Outline each blood parasite and name the species.
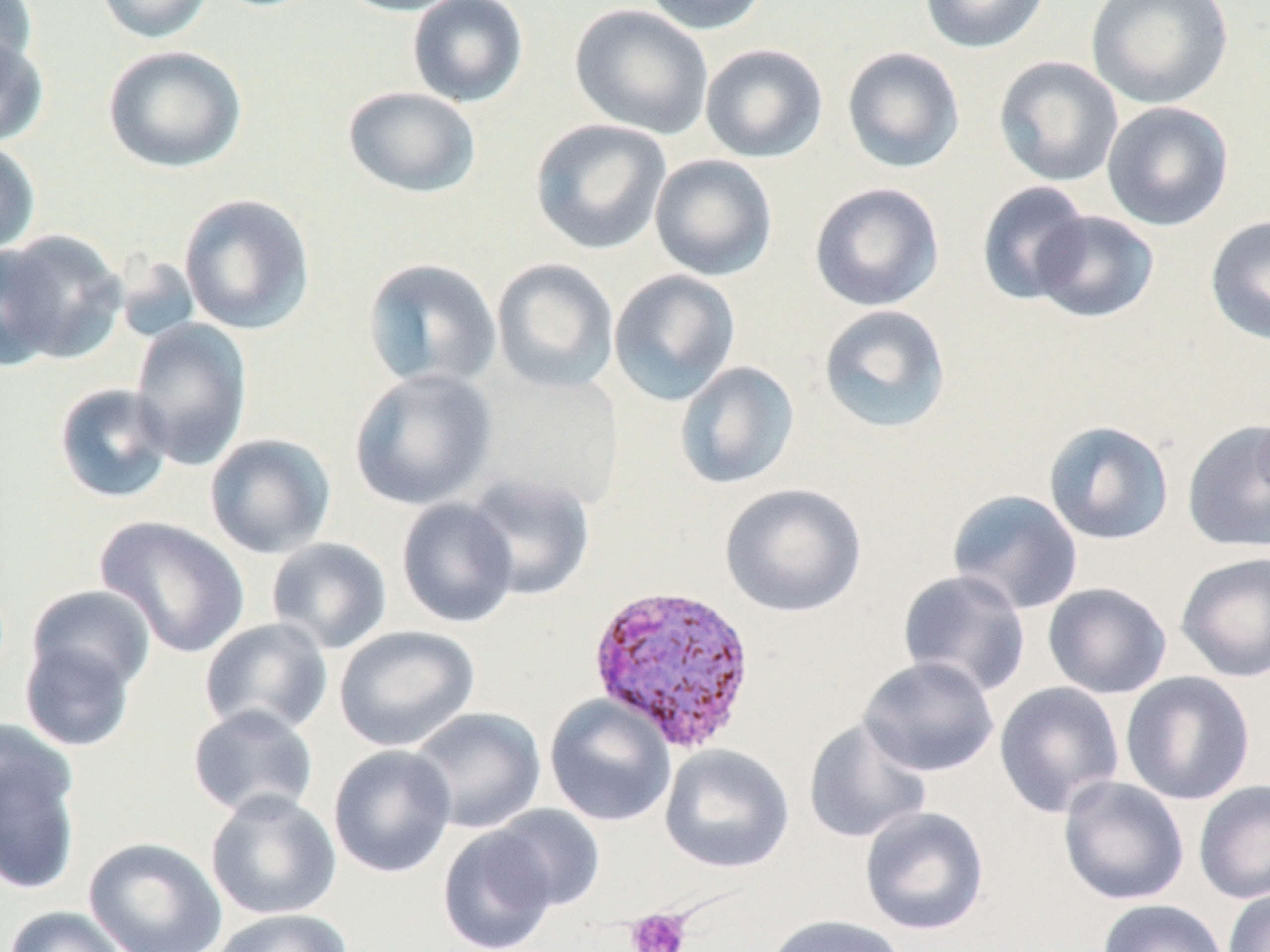
Approximate bounding boxes as (x1, y1, x2, y2) in pixels.
Plasmodium vivax-infected red blood cells: (587, 582, 758, 753).
No Plasmodium falciparum, Plasmodium ovale, Plasmodium malariae, Babesia divergens, or Trypanosoma brucei observed.

slide-level diagnosis = Plasmodium vivax
field of view = single
uninfected red blood cell locations = approximate bounding boxes as (x1, y1, x2, y2) in pixels: (0, 0, 39, 82), (95, 0, 214, 44), (335, 0, 472, 17), (407, 0, 529, 107), (642, 0, 771, 35), (918, 0, 1051, 54), (1086, 1, 1234, 109), (569, 4, 713, 139), (0, 33, 49, 148), (700, 43, 829, 163), (102, 44, 247, 173), (841, 46, 966, 173), (993, 56, 1125, 188), (342, 86, 482, 198), (1101, 101, 1234, 231), (529, 118, 672, 255), (0, 139, 41, 256), (649, 153, 779, 282), (976, 180, 1092, 306), (808, 182, 945, 312), (178, 193, 316, 335), (1030, 210, 1159, 324), (1205, 215, 1270, 347), (0, 230, 126, 366), (0, 240, 63, 374), (362, 257, 502, 391), (491, 257, 620, 394), (608, 269, 741, 407), (817, 304, 952, 435), (130, 318, 253, 470), (674, 361, 800, 490), (471, 366, 625, 513), (349, 367, 498, 511), (53, 383, 175, 504), (1182, 419, 1270, 553), (1042, 420, 1174, 545), (204, 433, 337, 560), (463, 473, 596, 602), (719, 483, 868, 618), (946, 489, 1084, 615), (396, 497, 520, 628), (94, 516, 249, 658), (265, 537, 393, 655), (1175, 551, 1270, 682), (897, 569, 1031, 698), (1042, 582, 1172, 699), (24, 584, 156, 696), (198, 617, 334, 737), (333, 625, 480, 752), (18, 637, 138, 752), (858, 656, 999, 778), (1119, 671, 1256, 806), (994, 681, 1125, 819), (544, 694, 676, 827), (187, 704, 319, 820), (407, 706, 547, 834), (803, 717, 932, 844), (0, 722, 83, 896), (659, 743, 794, 873), (327, 744, 457, 879), (1057, 775, 1190, 906), (1193, 779, 1270, 905), (204, 788, 341, 920), (487, 804, 605, 912), (859, 805, 990, 936), (437, 826, 559, 952), (83, 836, 228, 952), (1223, 887, 1270, 952), (1097, 898, 1229, 952), (2, 905, 132, 952), (208, 907, 354, 952), (762, 914, 909, 952)
modality = light microscopy
preparation = thin blood smear
platelet locations = approximate bounding boxes as (x1, y1, x2, y2) in pixels: (627, 907, 691, 952)
stain = May-Grünwald-Giemsa
magnification = 1000x
image size = 1270×952 pixels